Outline each Plasmodium parasite.
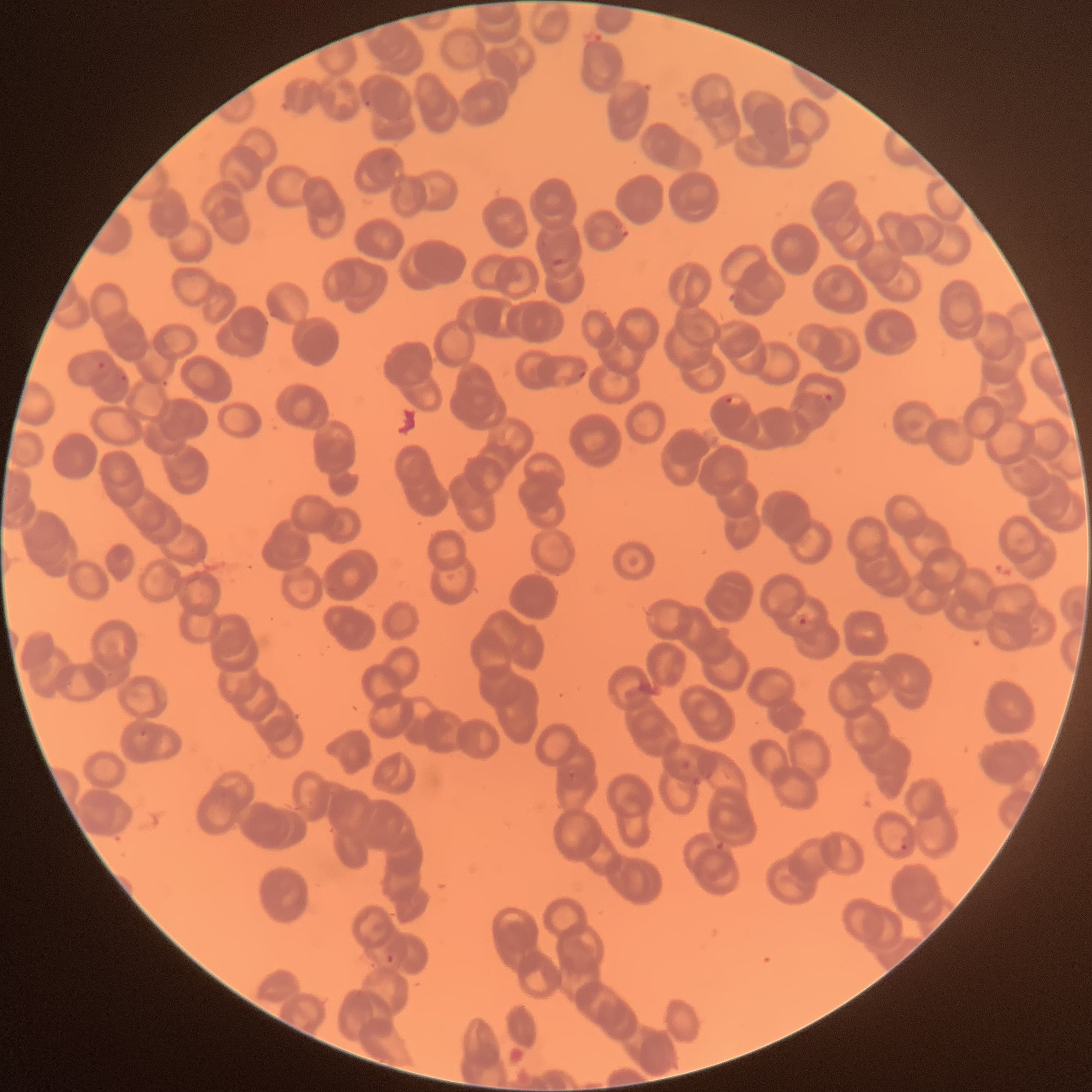

Approximate bounding boxes as (x1,y1)-(x2,y2) corner pairs in pixels.
Plasmodium parasites: (363,100)-(374,109), (552,256)-(565,267), (98,362)-(106,370), (579,370)-(586,379), (119,374)-(128,382), (823,392)-(835,402), (725,396)-(743,407), (798,617)-(806,625), (139,729)-(148,737), (567,771)-(578,782), (899,842)-(912,854), (385,954)-(396,964).

image_size: 1092×1092 pixels
preparation: thin blood film
modality: optical microscopy
red_blood_cell_morphology: rouleaux formation